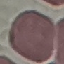
Summary:
  - Malaria status: uninfected
  - Preparation: thin smear
  - Capture: smartphone through the microscope eyepiece
  - Stain: Giemsa
  - Image type: automatically extracted cell patch, resized to 64 × 64 pixels